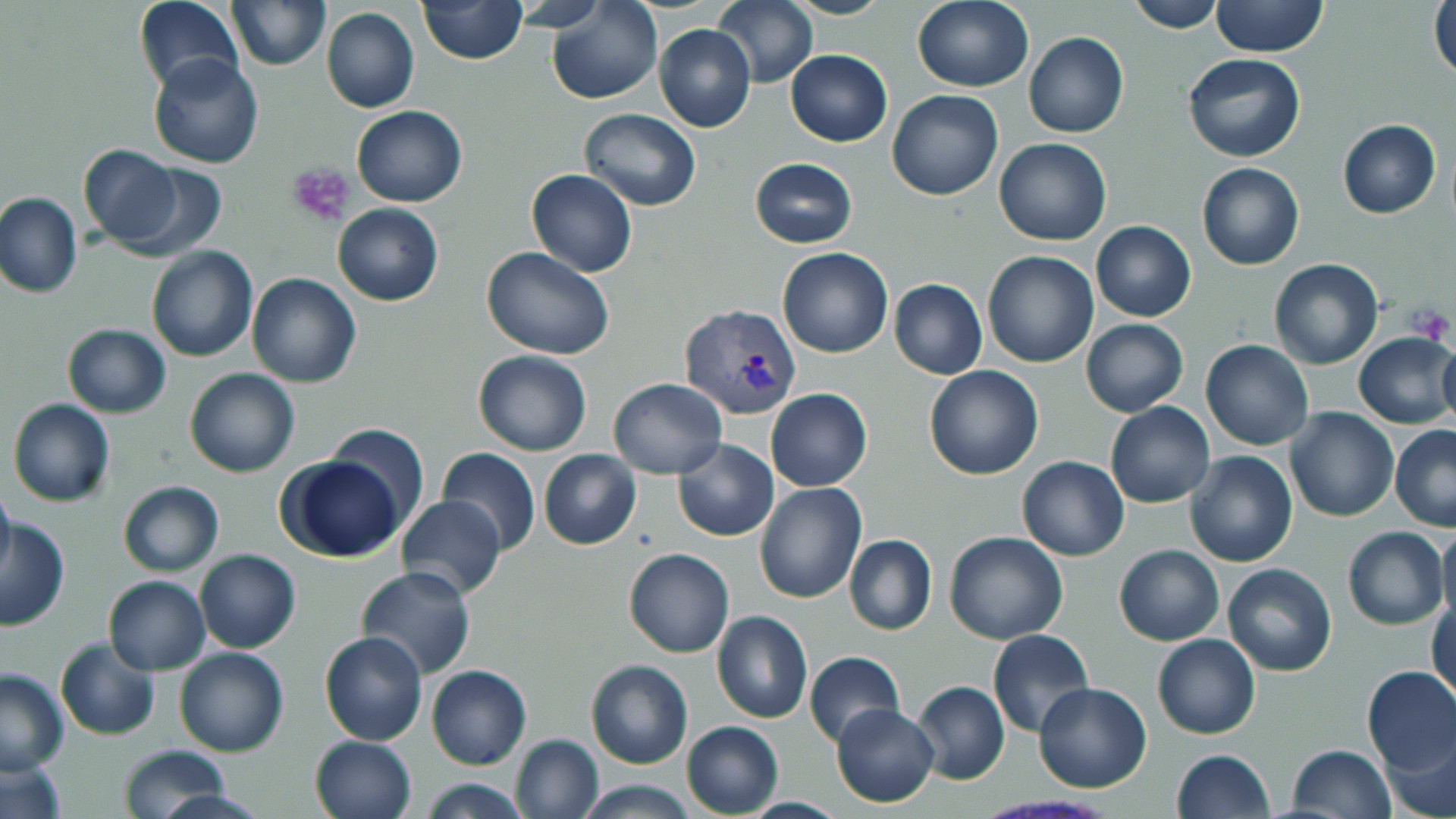
Summary:
  - Coordinate format: approximate bounding boxes as (x1,y1)-(x2,y2) corner pairs in pixels
  - Platelet locations: (287,163)-(356,228), (1409,305)-(1454,344)
  - Uninfected red blood cell locations: (134,0)-(242,96), (418,0)-(525,64), (546,0)-(662,104), (714,0)-(819,88), (1124,0)-(1226,33), (1211,0)-(1328,59), (1429,0)-(1456,87), (227,1)-(330,70), (912,1)-(1033,92), (321,7)-(419,114), (654,24)-(756,132), (1024,32)-(1128,137), (786,49)-(892,146), (148,51)-(264,168), (1183,54)-(1306,162), (886,90)-(1003,201), (351,105)-(468,207), (577,109)-(702,210), (1337,119)-(1440,218), (993,138)-(1112,246), (77,145)-(186,249), (751,157)-(858,249), (1197,162)-(1304,270), (116,164)-(226,261), (526,169)-(637,276), (0,193)-(83,298), (333,203)-(444,307), (1091,221)-(1196,322), (481,244)-(616,360), (146,246)-(258,363), (777,247)-(893,359), (982,250)-(1100,367), (159,258)-(356,373), (1268,258)-(1384,370), (246,273)-(360,388), (889,279)-(988,379), (1081,319)-(1187,416), (62,323)-(170,418), (1354,331)-(1456,429), (1200,339)-(1314,451), (1437,341)-(1456,429), (472,349)-(595,456), (924,366)-(1044,480), (185,368)-(301,478), (608,378)-(727,477), (765,388)-(872,491), (6,398)-(115,507), (1106,401)-(1215,508), (1284,407)-(1399,523), (324,425)-(429,537), (1389,425)-(1456,532), (672,439)-(778,541), (438,447)-(541,554), (538,449)-(640,549), (1186,451)-(1298,568), (1017,456)-(1129,560), (282,458)-(404,562), (118,480)-(224,576), (754,482)-(865,604), (0,483)-(13,580), (396,494)-(505,601), (0,519)-(70,630), (1437,522)-(1456,626), (1343,527)-(1448,630), (945,531)-(1068,643), (844,535)-(937,636), (1114,544)-(1224,646), (622,548)-(735,658), (194,549)-(300,653), (1222,563)-(1336,677), (355,565)-(475,680), (103,575)-(211,674), (1429,593)-(1455,705), (712,610)-(813,724), (987,628)-(1093,738), (319,632)-(427,745), (1153,634)-(1259,739), (54,638)-(161,741), (173,646)-(289,758), (804,651)-(905,747), (585,660)-(693,769), (426,664)-(531,768), (1360,666)-(1456,775), (0,668)-(69,774), (911,681)-(1009,785), (1033,681)-(1152,793), (831,703)-(940,807), (682,721)-(784,817), (1375,729)-(1456,819), (509,733)-(604,819), (310,734)-(417,819), (1285,744)-(1396,817), (116,746)-(234,815), (1171,749)-(1275,819), (1,753)-(67,819), (416,778)-(533,817), (574,780)-(702,816)
  - Plasmodium vivax-infected red blood cell locations: (679,304)-(801,418)
  - Slide-level diagnosis: Plasmodium vivax
  - Image size: 1456×819 pixels
  - Field of view: single
  - Stain: May-Grünwald-Giemsa
  - Magnification: 1000x
  - Modality: light microscopy
  - Preparation: thin blood smear